Comment on the morphology of the red blood cells.
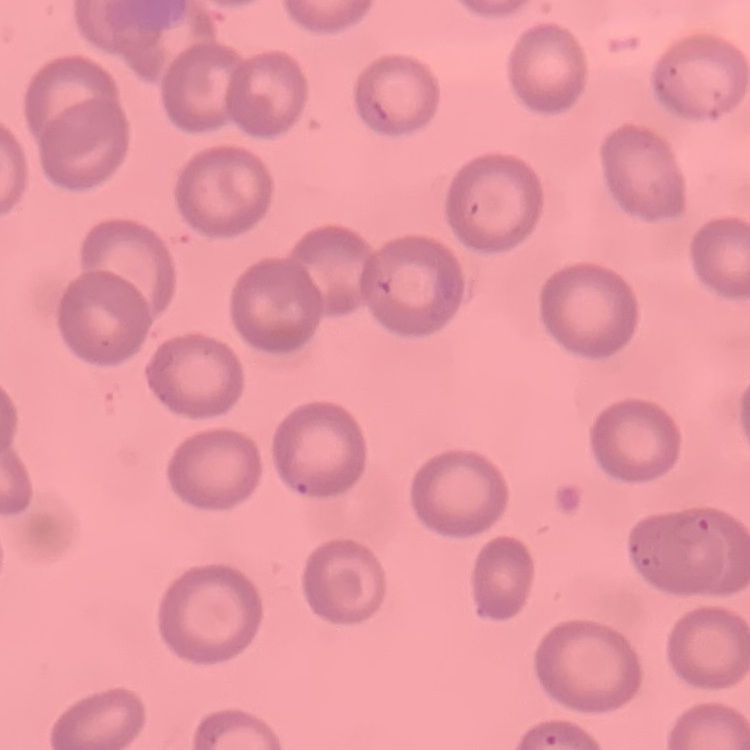
They show no rouleaux formation.

image_type: one tile cut from a larger photomicrograph
stain: Field's or Giemsa
preparation: thin peripheral smear